Point out each leukocyte.
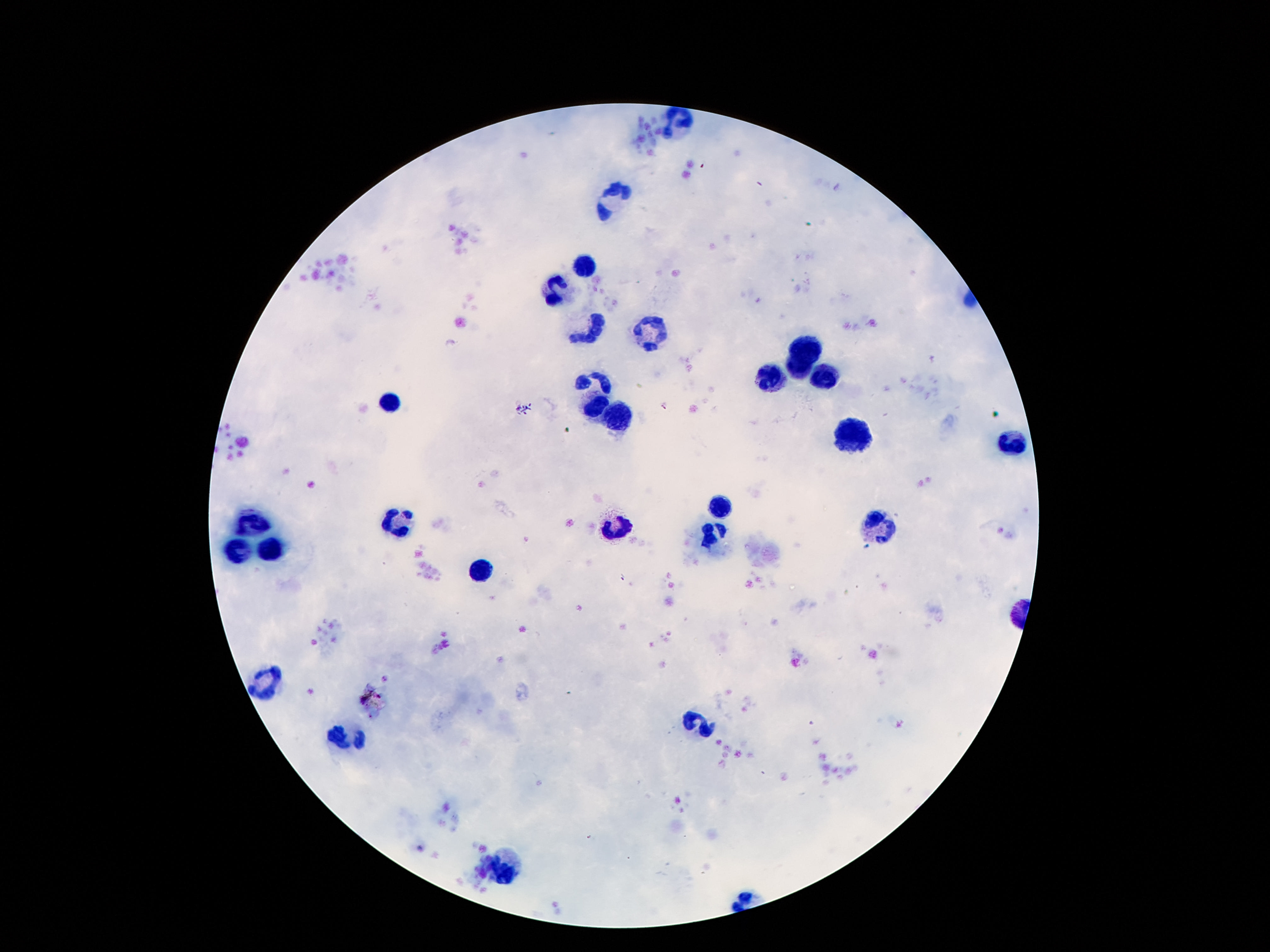
Approximate centers as [x, y] in pixels.
Leukocytes: [677, 123], [614, 198], [583, 266], [553, 289], [588, 333], [651, 334], [810, 342], [798, 373], [821, 378], [773, 379], [593, 380], [387, 401], [593, 408], [614, 417], [851, 436], [1017, 446], [725, 507], [398, 521], [879, 521], [252, 522], [616, 529], [712, 536], [238, 552], [276, 552], [480, 569], [264, 680], [700, 720], [345, 738], [504, 871].

Summary:
  - Stain: Giemsa
  - Field of view: one from this slide
  - Capture: smartphone camera through the microscope eyepiece
  - Magnification: 100x
  - Preparation: thick blood smear
  - Image size: 1270×952 pixels
  - Patient malaria status: uninfected